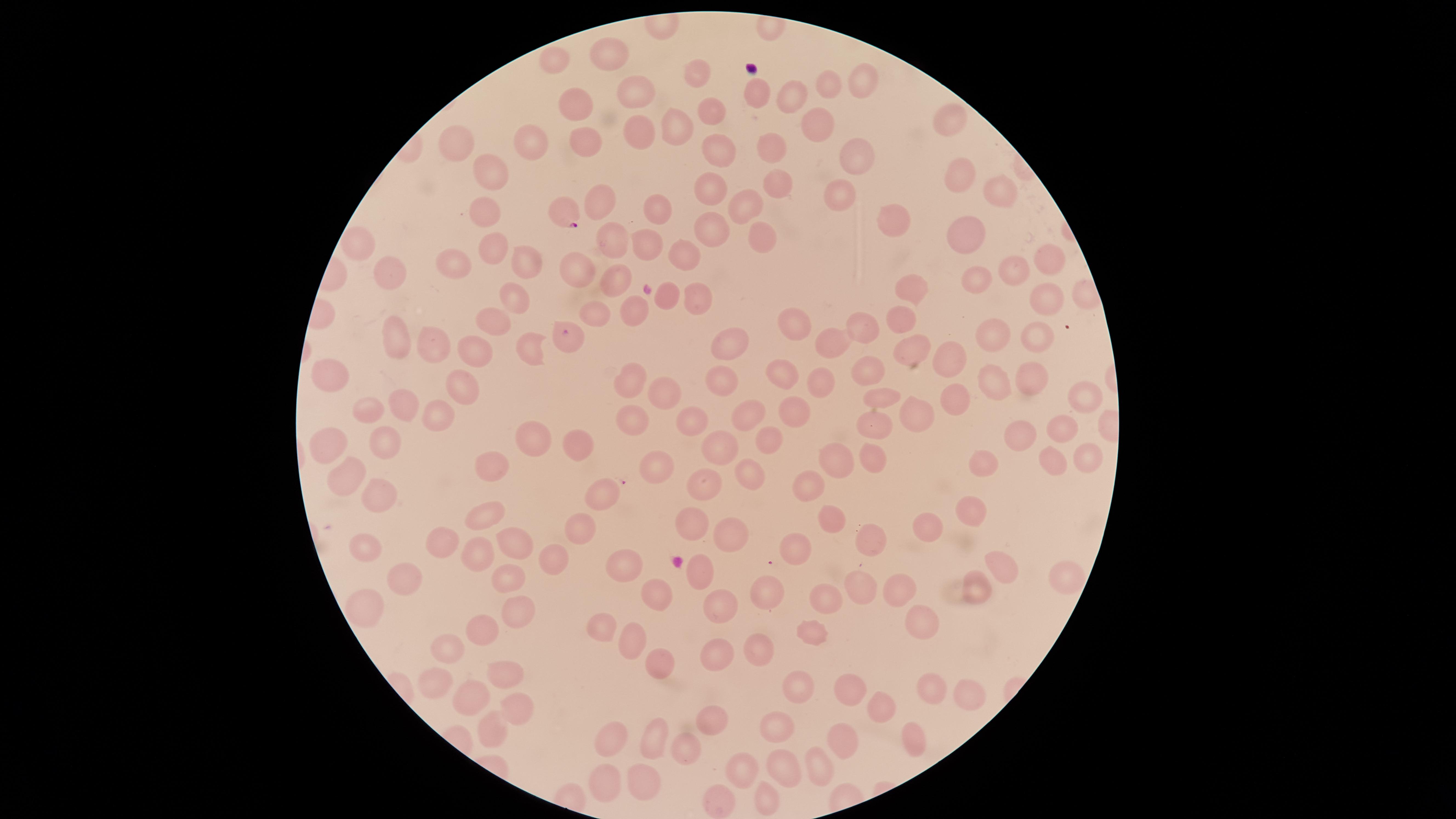

species: Plasmodium falciparum
presence: malaria parasites seen
stain: Giemsa
preparation: thin blood film
uninfected_red_blood_cells: 'approximate marker points as (x, y) in pixels: (608, 55), (555, 56), (700, 78), (862, 82), (824, 85), (758, 93), (796, 94), (636, 95), (582, 107), (713, 114), (952, 119), (814, 122), (677, 124), (638, 135), (532, 143), (586, 146), (765, 146), (464, 147), (721, 150), (855, 154), (489, 173), (955, 177), (710, 187), (778, 188), (998, 193), (840, 197), (598, 202), (742, 204), (649, 209), (485, 211), (890, 218), (972, 225), (713, 230), (612, 239), (760, 239), (649, 240), (360, 242), (488, 250), (684, 253), (1051, 261), (527, 263), (454, 266), (581, 267), (393, 271), (1013, 271), (974, 274), (616, 280), (908, 285), (670, 294), (696, 295), (1049, 298), (507, 300), (598, 306), (636, 312), (901, 315), (493, 323), (798, 323), (864, 327), (1042, 334), (400, 337), (999, 337), (735, 340), (439, 343), (834, 345), (910, 345), (528, 346), (479, 349), (956, 357), (785, 369), (872, 372), (332, 375), (721, 377), (1028, 380), (463, 381), (637, 381), (822, 383), (993, 385), (1083, 394), (664, 395), (883, 395), (955, 396), (404, 406), (748, 409), (370, 410), (795, 411), (629, 414), (917, 414), (435, 415), (877, 417), (698, 420), (1060, 427), (1025, 431), (771, 439), (533, 441), (577, 442), (329, 446), (385, 446), (721, 446), (1084, 454), (872, 457), (984, 458), (835, 459), (1052, 459), (489, 464), (657, 464), (750, 472), (345, 479), (701, 482), (807, 488), (374, 495), (605, 497), (968, 511), (483, 512), (829, 516), (688, 520), (929, 525), (577, 532), (728, 535), (443, 536), (873, 541), (797, 543), (511, 544), (363, 547), (479, 551), (554, 558), (623, 562), (695, 570), (999, 570), (504, 575), (403, 576), (1064, 579), (978, 583), (854, 584), (890, 587), (768, 590), (654, 594), (713, 599), (824, 599), (364, 604), (518, 610), (920, 618), (605, 623), (483, 628), (812, 630), (636, 639), (763, 643), (446, 650), (718, 652), (663, 659), (509, 676), (802, 680), (440, 681), (930, 682), (848, 694), (965, 694), (470, 698), (878, 704), (515, 706), (713, 723), (782, 728), (492, 731), (842, 736), (909, 736), (613, 737), (654, 737), (688, 749), (819, 753), (781, 766), (742, 769), (644, 773), (599, 778), (766, 803), (717, 804)'
capture: smartphone photograph through the microscope eyepiece
field_of_view: single
image_size: 1456×819 pixels
parasitized_red_blood_cells: 'approximate marker points as (x, y) in pixels: (565, 211), (570, 338)'
visible_region: circular